Evaluate for Plasmodium parasites.
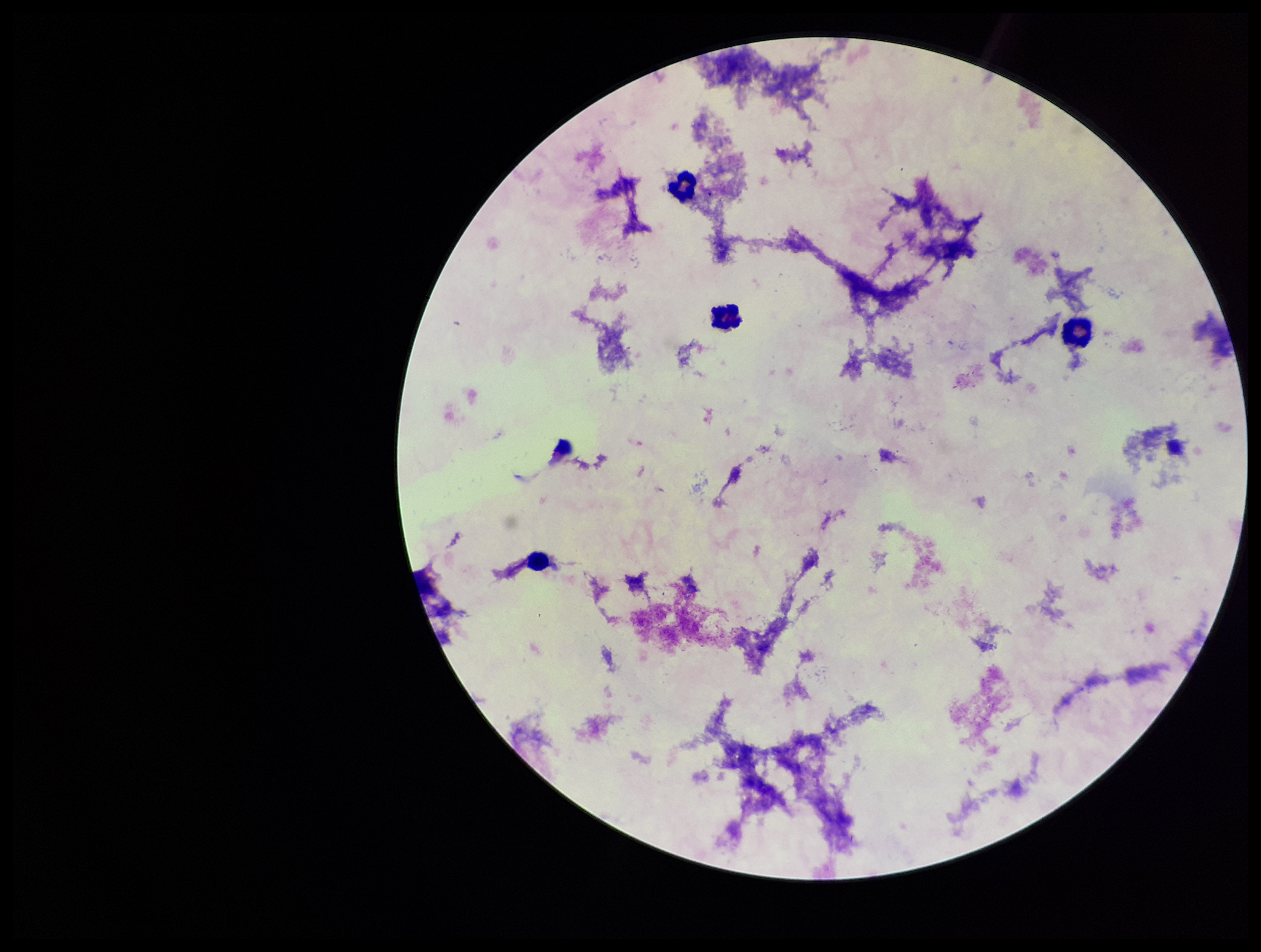

None identified.

Parasite count: 0. Leukocyte count: 4. Image is 1261×952 pixels. Preparation: thick blood smear. Photographed through the microscope eyepiece with a smartphone camera. Single field of view. Patient malaria status: negative. Giemsa stain.